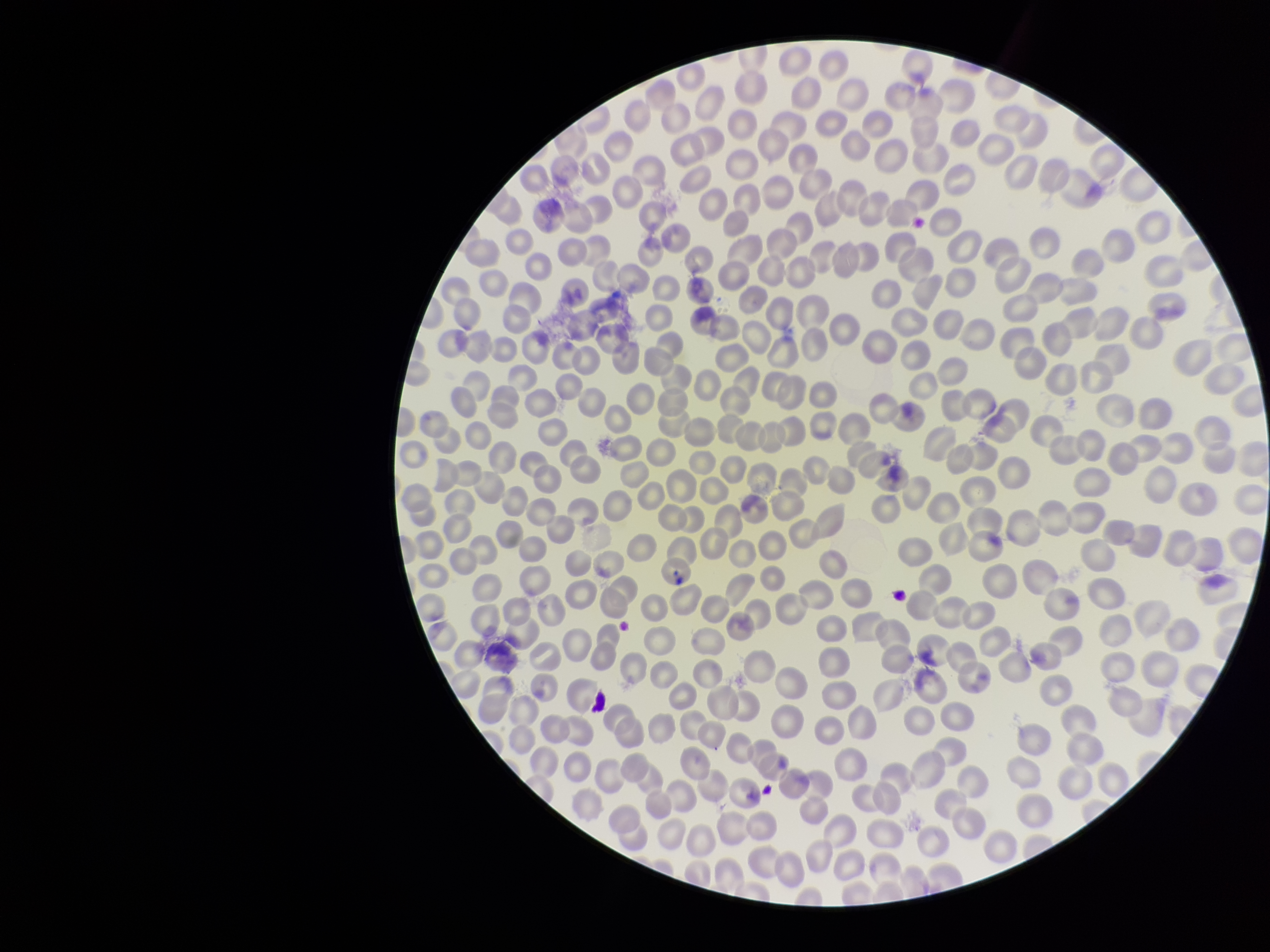

{
  "capture": "smartphone photograph through the microscope eyepiece",
  "image_size": "1270×952 pixels",
  "red_blood_cell_count": 332,
  "preparation": "thin smear",
  "stain": "Giemsa",
  "parasitized_red_blood_cells": "none identified",
  "parasitized_red_blood_cell_count": 0,
  "field_of_view": "single",
  "patient_malaria_status": "negative"
}